Mark where leukocytes are.
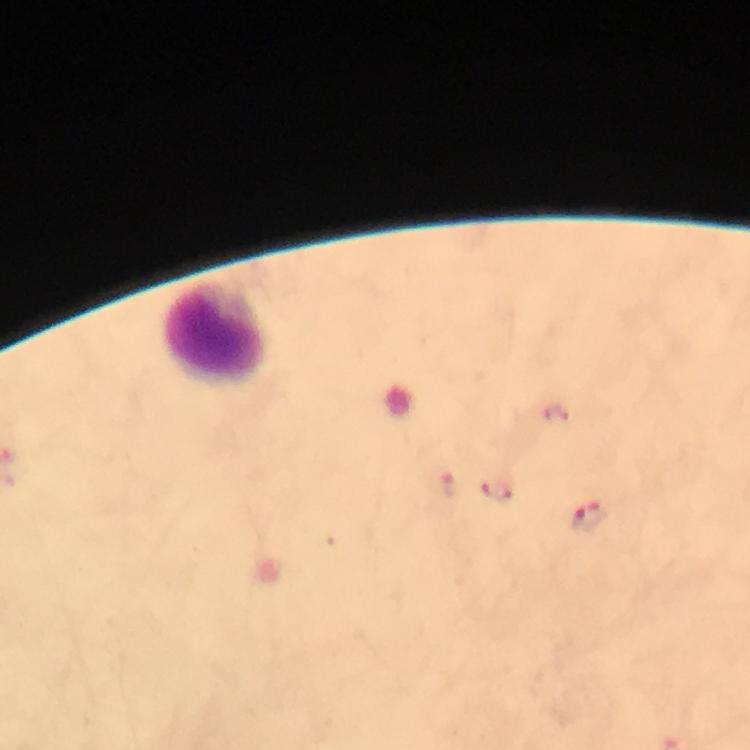

Approximate object centers, in pixels from the top-left corner.
Leukocytes: (x=213, y=332).

Malaria parasite locations: (x=555, y=413), (x=447, y=485), (x=496, y=490), (x=588, y=516). Giemsa-stained preparation. Photographed with a smartphone mounted on the microscope. Image is 750×750 pixels. From a malaria diagnostic workup. At 100x magnification. A crop from one field of view. Immersion oil applied. Thick blood smear.